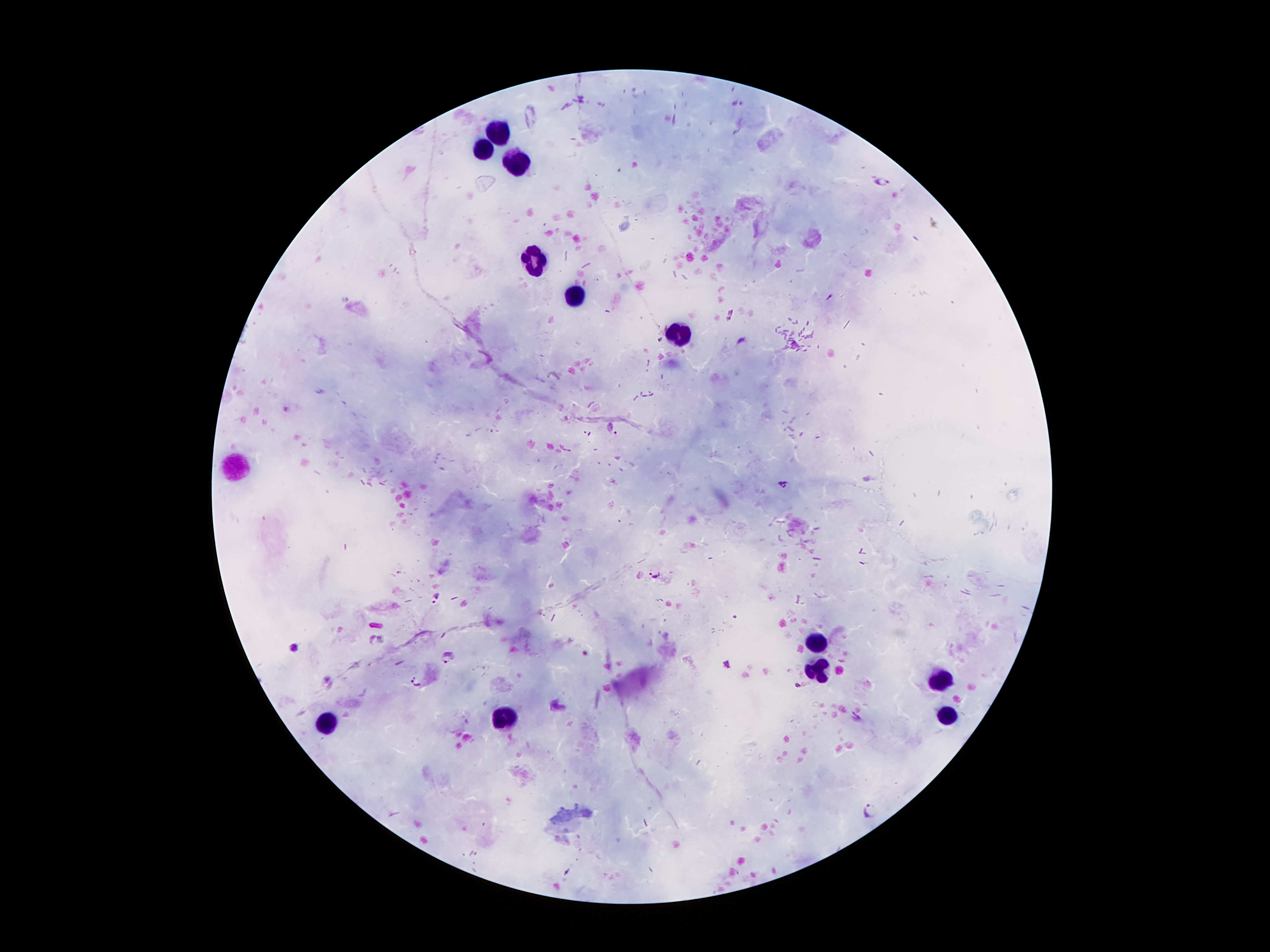

Approximate centers as (x, y) in pixels.
Summary:
  - Leukocyte locations: (500, 133), (485, 151), (514, 167), (531, 263), (575, 297), (676, 332), (236, 467), (816, 643), (821, 669), (944, 679), (509, 715), (951, 715), (328, 724)
  - Plasmodium parasite locations: (882, 180), (613, 429), (587, 433), (783, 485), (656, 573), (294, 648), (450, 656), (416, 683), (869, 810)
  - Preparation: thick peripheral-blood smear
  - Patient malaria status: infected with Plasmodium falciparum
  - Field of view: one from this slide
  - Capture: smartphone through the microscope eyepiece
  - Image size: 1270×952 pixels
  - Magnification: 100x
  - Stain: Giemsa